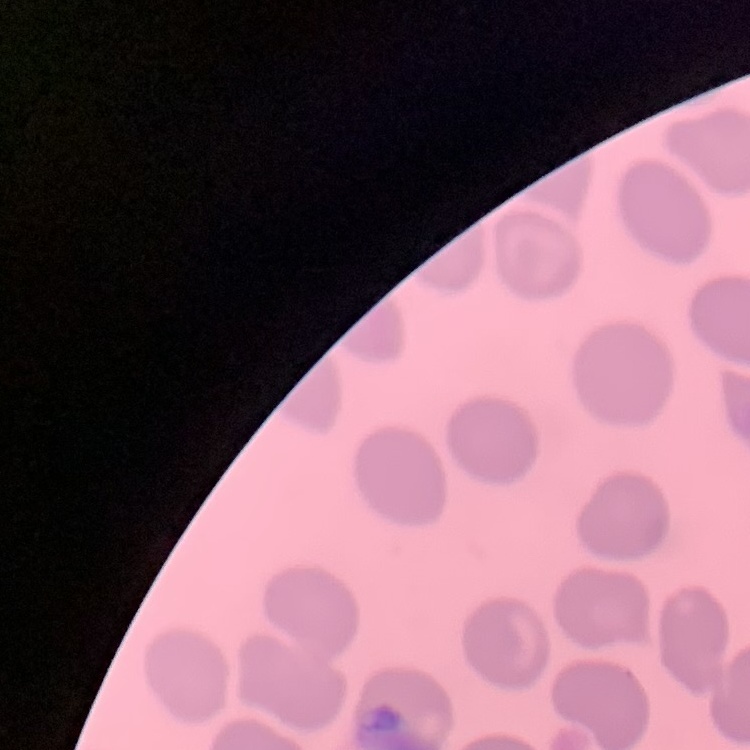

The erythrocytes show no rouleaux formation. Thin blood film. One tile cut from a larger photomicrograph. Stained with either Field's or Giemsa.